Report the malaria status of this cell.
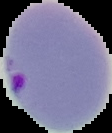
Parasitized.

image_size: 112×133 pixels
preparation: thin blood smear
image_type: segmented cell region on a black background